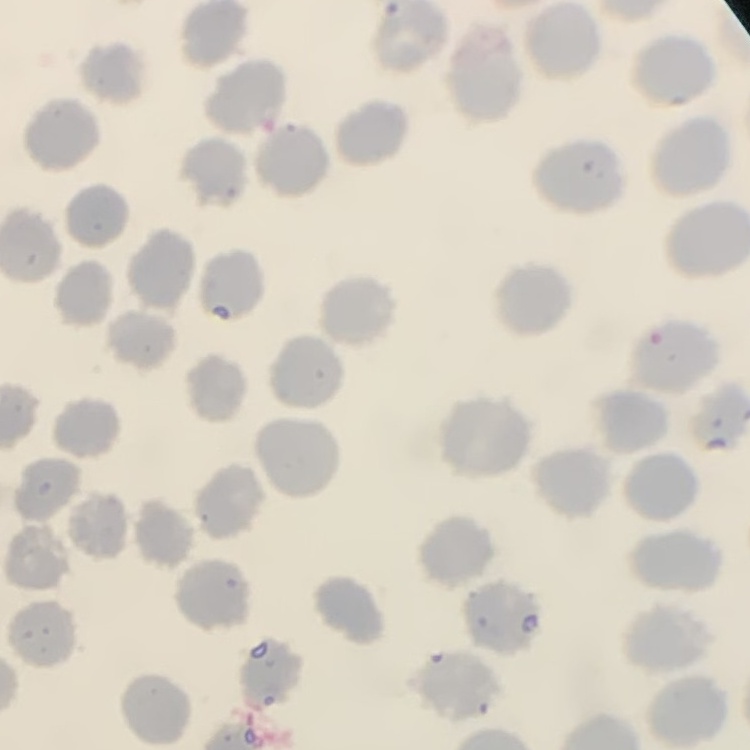

Summary:
  - Red blood cell morphology: no rouleaux formation
  - Image type: one tile cut from a larger photomicrograph
  - Preparation: thin blood film
  - Stain: Field's or Giemsa